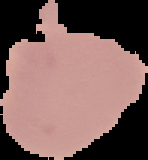

Result: negative for Plasmodium parasites. Cell region segmented out of the field of view; the surrounding area is masked to black. From a thin blood smear. Image is 148×160 pixels.